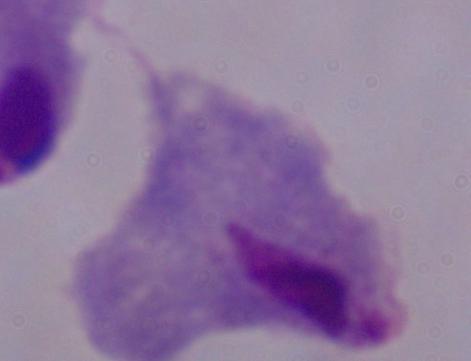
Summary:
  - Modality: photomicrograph
  - Identification: trichomonad
  - Magnification: 1000x